Assess the morphology of the erythrocytes.
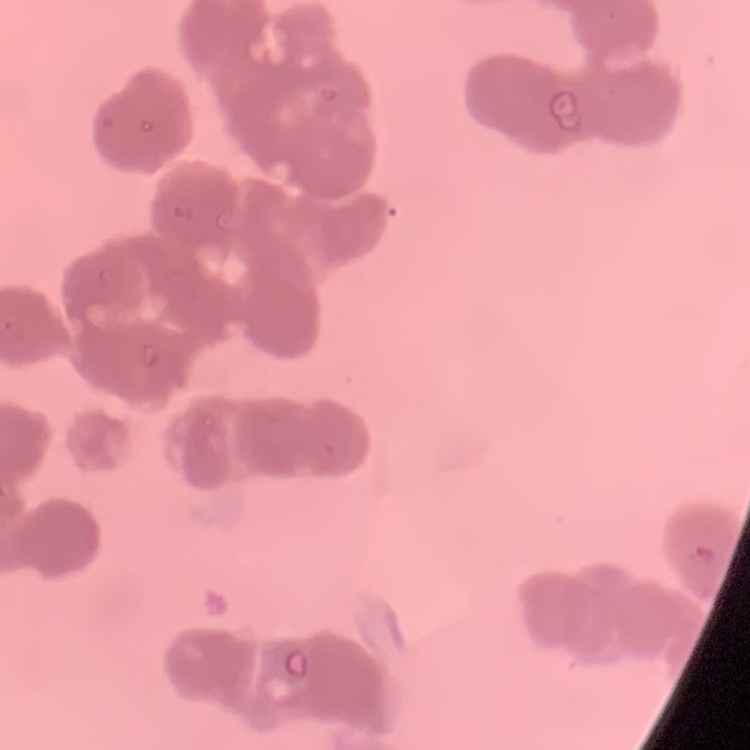

Rouleaux formation.

preparation: thin blood smear
image_type: square crop of a larger photomicrograph
stain: Field's or Giemsa